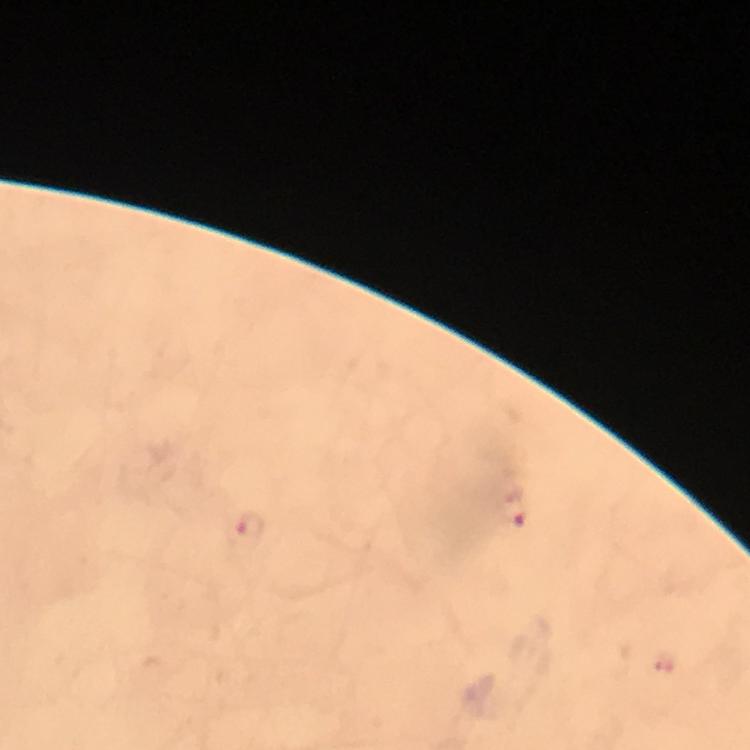

{
  "capture": "smartphone camera through the microscope",
  "malaria_parasite_locations": "approximate object centers, in pixels from the top-left corner: (x=514, y=508), (x=250, y=528)",
  "preparation": "thick blood film",
  "stain": "Giemsa",
  "context": "from a malaria diagnostic workup",
  "image_size": "750×750 pixels",
  "immersion_oil": "applied",
  "cropped_from": "a single field of view",
  "magnification": "100x"
}